Outline each uninfected red blood cell.
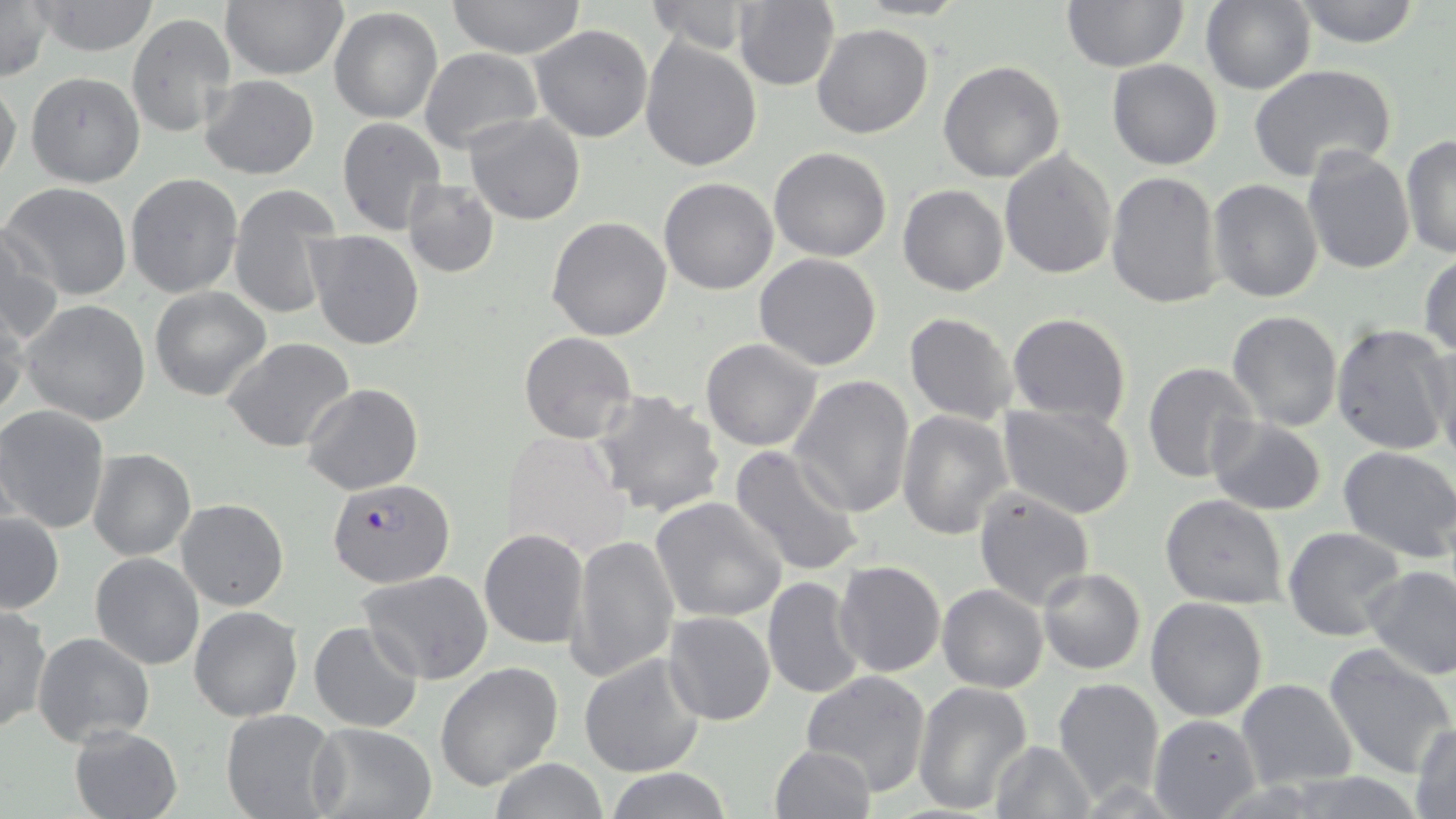
Approximate bounding boxes as [x1, y1, x2, y2] in pixels.
Uninfected red blood cells: [220, 0, 349, 80], [447, 0, 587, 60], [734, 0, 840, 91], [1059, 0, 1189, 71], [1293, 0, 1423, 48], [0, 1, 54, 81], [30, 1, 161, 56], [646, 1, 756, 55], [1200, 1, 1314, 93], [329, 7, 443, 125], [126, 12, 237, 140], [811, 21, 934, 139], [529, 24, 654, 144], [640, 38, 762, 173], [420, 48, 543, 155], [938, 59, 1068, 184], [1106, 59, 1223, 170], [1248, 64, 1398, 182], [25, 71, 145, 188], [199, 74, 320, 180], [0, 79, 22, 187], [464, 112, 586, 225], [337, 118, 447, 238], [1401, 134, 1456, 259], [769, 146, 892, 261], [1300, 146, 1415, 277], [1000, 149, 1118, 280], [1105, 170, 1222, 309], [125, 173, 242, 299], [659, 176, 778, 295], [1208, 178, 1324, 302], [403, 179, 500, 277], [3, 181, 134, 301], [227, 184, 341, 321], [898, 184, 1008, 296], [547, 216, 672, 340], [1, 227, 65, 345], [304, 230, 425, 351], [1418, 253, 1455, 361], [754, 254, 883, 370], [148, 287, 271, 401], [20, 300, 152, 426], [0, 303, 29, 422], [1226, 309, 1343, 431], [1005, 311, 1131, 427], [903, 312, 1018, 425], [1330, 323, 1453, 453], [519, 331, 636, 445], [1425, 333, 1455, 461], [223, 337, 357, 453], [700, 339, 823, 452], [1141, 361, 1262, 485], [788, 375, 915, 518], [301, 384, 422, 496], [591, 388, 727, 519], [999, 401, 1136, 518], [0, 405, 110, 534], [897, 410, 1012, 540], [1205, 414, 1329, 515], [500, 430, 631, 560], [730, 444, 866, 580], [1338, 447, 1456, 562], [87, 449, 196, 562], [973, 486, 1095, 610], [1160, 493, 1289, 608], [649, 496, 789, 624], [176, 499, 289, 610], [1, 512, 65, 615], [1282, 527, 1408, 642], [479, 529, 588, 649], [568, 532, 680, 683], [90, 552, 204, 670], [832, 560, 945, 678], [1363, 563, 1456, 680], [1037, 567, 1146, 675], [356, 570, 495, 685], [762, 576, 865, 699], [937, 584, 1048, 693], [1144, 596, 1270, 722], [0, 604, 50, 734], [188, 605, 303, 722], [664, 612, 777, 726], [308, 622, 422, 733], [33, 632, 157, 748], [1323, 645, 1455, 779], [579, 653, 707, 778], [435, 663, 565, 790], [800, 669, 932, 796], [1052, 677, 1165, 804], [1234, 678, 1359, 791], [912, 682, 1033, 815], [221, 706, 341, 819], [1149, 713, 1260, 819], [308, 721, 439, 819], [1410, 723, 1455, 818], [68, 725, 183, 819], [988, 739, 1095, 818], [768, 744, 876, 819], [487, 759, 611, 819], [601, 767, 730, 819].

slide-level diagnosis = Plasmodium falciparum
stain = May-Grünwald-Giemsa
Plasmodium falciparum-infected red blood cell locations = approximate bounding boxes as [x1, y1, x2, y2] in pixels: [326, 480, 456, 588]
field of view = one of a larger specimen
preparation = thin blood smear
magnification = 1000x
image size = 1456×819 pixels
modality = optical microscopy